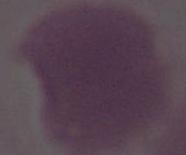
magnification = 1000x
identification = red blood cell
modality = micrograph